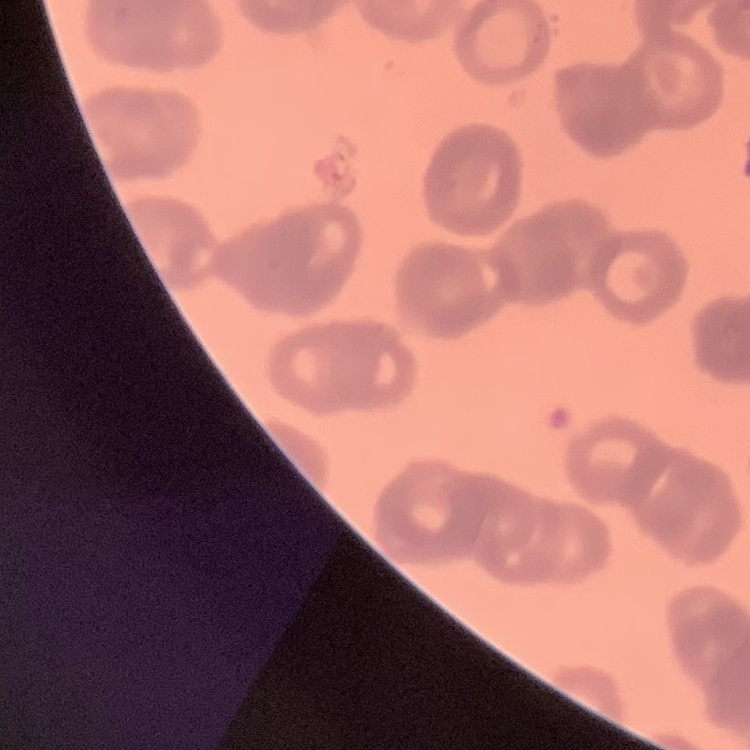

Summary:
  - Erythrocyte morphology: rouleaux formation
  - Preparation: thin blood smear
  - Image type: square crop of a larger photomicrograph
  - Stain: Field's or Giemsa